Point out each Plasmodium parasite.
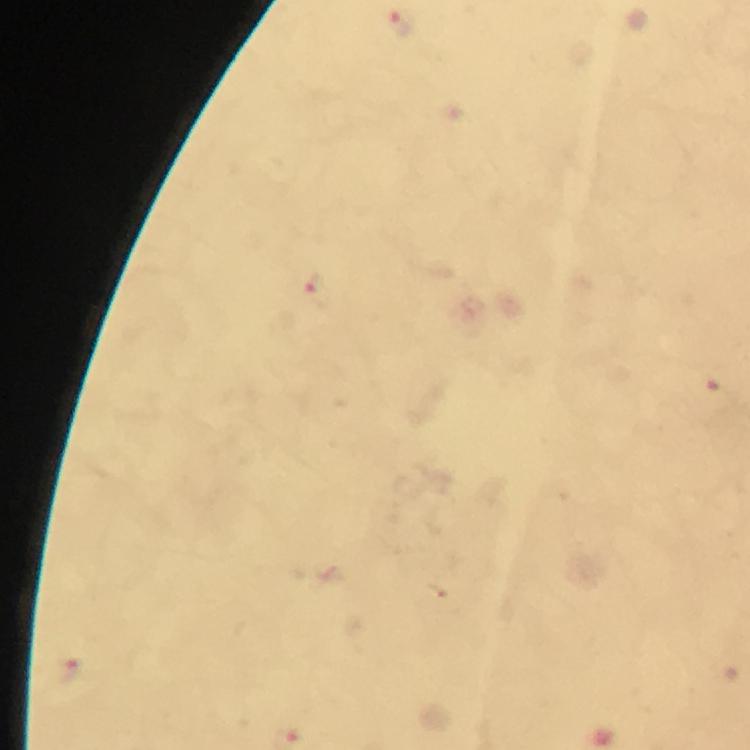

Approximate object centers, in pixels from the top-left corner.
Plasmodium parasites: (x=396, y=24), (x=316, y=294), (x=70, y=673).

Cropped region of a single field of view. Photographed with a smartphone mounted on the microscope. Thick blood smear. Image is 750×750 pixels. Giemsa-stained preparation. 100x magnification. From a malaria diagnostic workup. Immersion oil applied.